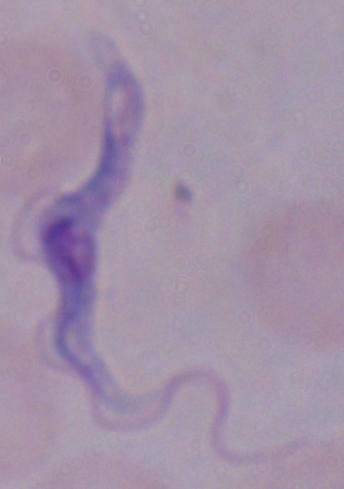
Summary:
  - Magnification: 1000x
  - Identification: trypanosome
  - Modality: photomicrograph